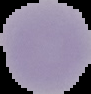
{
  "preparation": "thin blood smear",
  "image_size": "91×94 pixels",
  "malaria_status": "uninfected",
  "image_type": "cell region segmented out of the field of view; surrounding area masked to black"
}